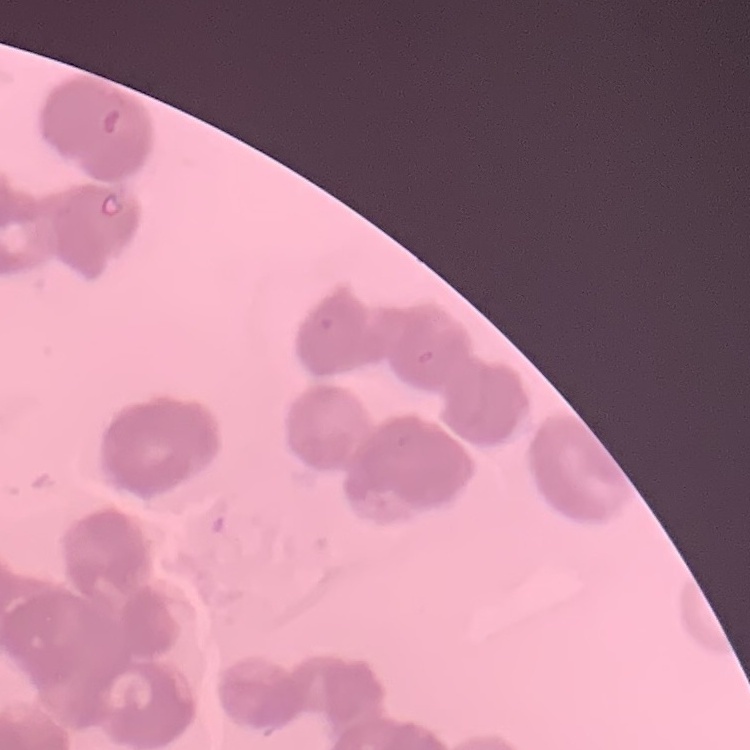
Summary:
  - Red blood cell morphology: rouleaux formation
  - Preparation: thin blood smear
  - Stain: Field's or Giemsa
  - Image type: one tile cut from a larger photomicrograph